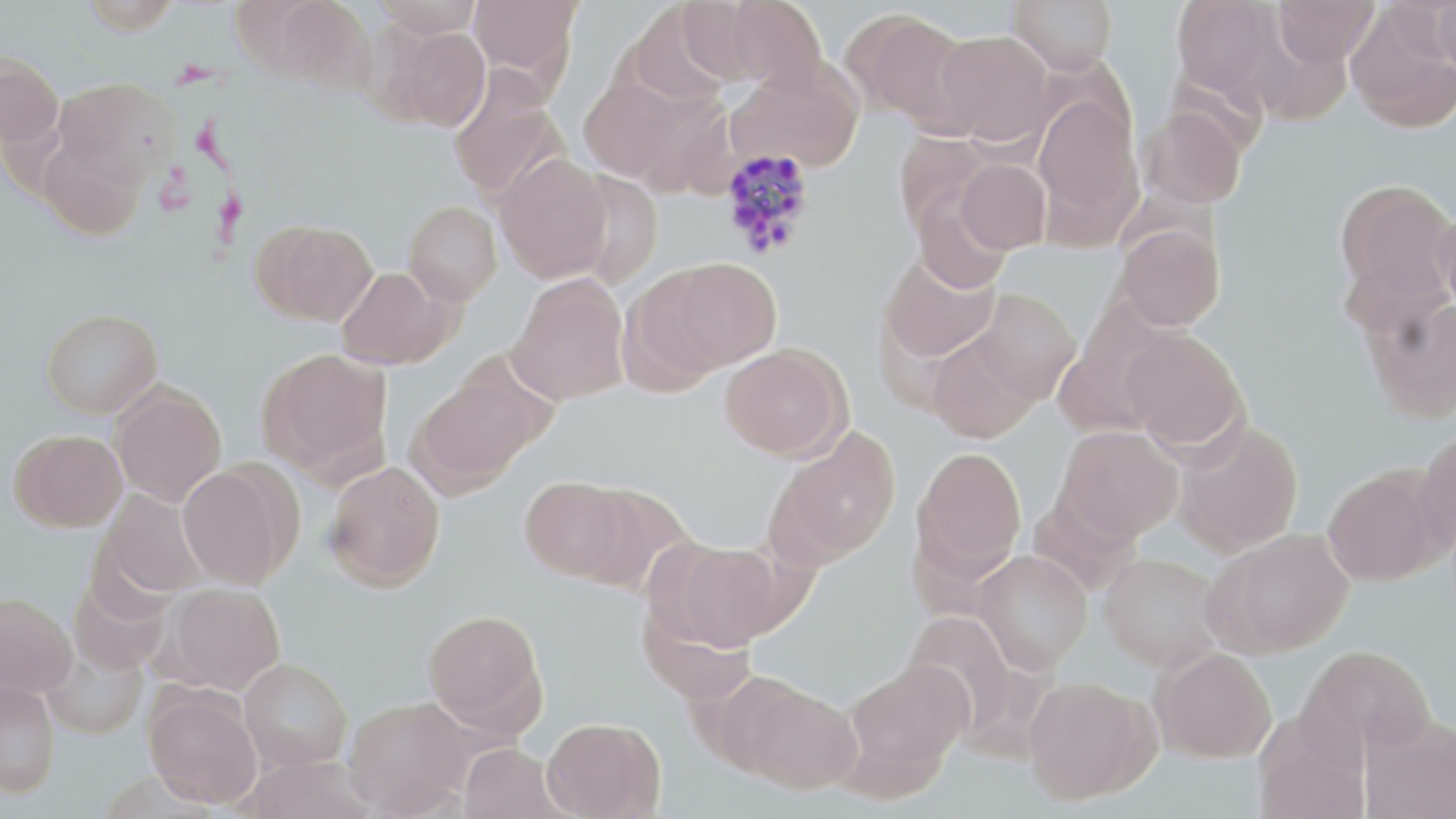
Approximate bounding boxes as (x1, y1, x2, y2) in pixels. Plasmodium vivax-infected red blood cell locations: (719, 147, 818, 260). Uninfected red blood cell locations: (267, 0, 376, 93), (372, 0, 484, 37), (468, 0, 581, 86), (716, 0, 828, 91), (1008, 0, 1118, 74), (1170, 0, 1281, 97), (1272, 0, 1379, 68), (1432, 0, 1456, 73), (624, 4, 734, 108), (1345, 5, 1455, 132), (844, 8, 976, 131), (387, 26, 493, 131), (933, 29, 1055, 145), (0, 56, 63, 149), (727, 64, 865, 171), (54, 77, 182, 188), (448, 77, 569, 204), (579, 78, 683, 181), (1032, 95, 1142, 235), (1138, 106, 1247, 209), (37, 136, 147, 241), (495, 153, 612, 283), (956, 158, 1050, 254), (566, 171, 663, 290), (1333, 177, 1456, 315), (910, 185, 1013, 293), (403, 201, 502, 305), (1436, 208, 1456, 324), (252, 218, 378, 326), (1113, 223, 1224, 332), (878, 252, 1000, 364), (653, 256, 783, 375), (336, 266, 453, 370), (507, 275, 630, 404), (969, 288, 1081, 404), (1362, 295, 1456, 424), (41, 308, 163, 418), (1121, 326, 1248, 453), (926, 329, 1043, 442), (718, 343, 851, 460), (258, 347, 393, 475), (409, 368, 545, 493), (110, 382, 227, 506), (1173, 419, 1303, 557), (1056, 426, 1184, 541), (767, 427, 901, 567), (8, 429, 127, 532), (1413, 430, 1456, 556), (912, 446, 1027, 580), (324, 460, 446, 591), (178, 463, 296, 589), (1322, 465, 1447, 586), (519, 475, 633, 581), (571, 484, 689, 594), (99, 490, 208, 598), (1207, 528, 1355, 656), (653, 537, 786, 653), (973, 550, 1092, 673), (1098, 552, 1226, 671), (161, 582, 285, 694), (0, 593, 76, 697), (422, 609, 546, 734), (1298, 644, 1436, 761), (42, 645, 148, 740), (1151, 648, 1276, 762), (841, 657, 972, 791), (239, 658, 353, 770), (722, 674, 864, 795), (1023, 676, 1158, 805), (0, 680, 60, 798), (143, 685, 263, 808), (345, 696, 474, 816), (1251, 712, 1369, 819), (1361, 715, 1456, 819), (542, 716, 666, 818), (458, 743, 568, 818), (240, 755, 376, 818). Slide-level diagnosis: Plasmodium vivax. Thin blood smear. May-Grünwald-Giemsa-stained preparation. 1000x magnification. Image is 1456×819 pixels. Light microscopy. Single field of view.